Identify the blood parasite species.
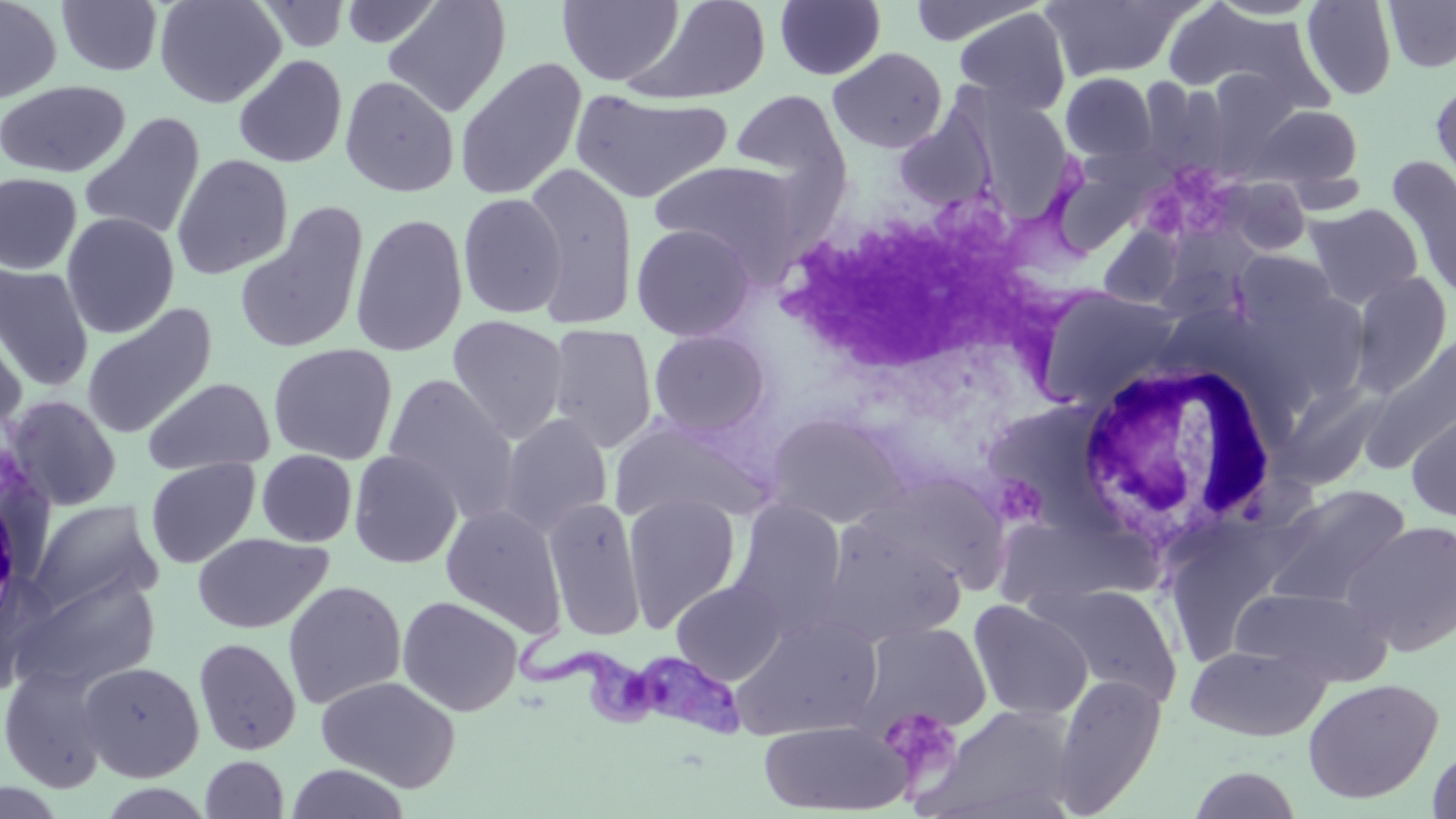
Trypanosoma brucei.

Summary:
  - Coordinate format: approximate bounding boxes as [x1, y1, x2, y2] in pixels
  - White blood cell locations: [768, 183, 1078, 387], [1072, 356, 1283, 562]
  - Platelet locations: [879, 706, 963, 787]
  - Uninfected red blood cell locations: [0, 0, 62, 104], [154, 0, 286, 109], [382, 0, 511, 118], [557, 0, 684, 87], [625, 0, 772, 106], [1040, 0, 1195, 82], [1206, 0, 1324, 20], [1301, 0, 1397, 100], [1384, 0, 1456, 73], [56, 1, 164, 76], [254, 1, 353, 52], [341, 1, 442, 48], [775, 1, 886, 81], [906, 1, 1038, 47], [1161, 2, 1310, 99], [953, 8, 1072, 117], [828, 47, 948, 153], [233, 54, 348, 168], [454, 57, 587, 202], [1060, 72, 1158, 163], [340, 75, 459, 197], [0, 80, 131, 179], [1430, 81, 1456, 203], [569, 89, 732, 204], [730, 89, 850, 191], [972, 96, 1076, 215], [1248, 104, 1363, 189], [78, 111, 206, 241], [893, 111, 996, 211], [172, 153, 293, 279], [1041, 153, 1156, 258], [1387, 156, 1456, 303], [649, 160, 804, 276], [522, 164, 639, 328], [0, 172, 82, 275], [1214, 176, 1312, 257], [769, 181, 1052, 388], [457, 193, 567, 319], [234, 202, 369, 355], [1305, 203, 1423, 309], [61, 212, 180, 338], [350, 212, 468, 357], [631, 223, 757, 342], [1097, 225, 1183, 309], [1233, 250, 1338, 336], [0, 263, 95, 391], [1349, 270, 1453, 398], [1033, 288, 1184, 409], [82, 303, 217, 439], [0, 314, 28, 446], [447, 315, 569, 444], [546, 324, 658, 453], [648, 328, 772, 439], [1362, 334, 1456, 474], [268, 343, 398, 464], [382, 374, 520, 522], [143, 378, 275, 476], [1272, 382, 1391, 492], [4, 395, 122, 511], [1406, 402, 1456, 523], [765, 410, 909, 529], [499, 413, 613, 538], [607, 414, 772, 527], [256, 449, 358, 547], [348, 450, 463, 569], [145, 458, 260, 569], [854, 472, 1012, 590], [1262, 484, 1412, 609], [623, 493, 741, 630], [544, 496, 646, 642], [730, 497, 848, 633], [28, 499, 161, 616], [441, 505, 566, 638], [819, 517, 965, 646], [1343, 519, 1456, 656], [192, 533, 333, 633], [17, 574, 159, 691], [671, 579, 787, 684], [282, 580, 406, 709], [1037, 583, 1183, 709], [1231, 585, 1393, 686], [397, 596, 523, 716], [968, 599, 1093, 721], [730, 614, 883, 740], [857, 621, 992, 736], [194, 637, 301, 756], [1185, 644, 1330, 741], [78, 661, 205, 782], [1, 664, 111, 793], [1051, 674, 1167, 816], [316, 675, 460, 792], [1302, 677, 1444, 804], [925, 702, 1080, 818], [759, 719, 910, 814], [1426, 741, 1456, 818], [200, 755, 289, 818], [285, 763, 411, 819], [1187, 766, 1305, 819]
  - Trypanosoma brucei locations: [513, 620, 746, 739]
  - Magnification: 1000x
  - Stain: May-Grünwald-Giemsa
  - Preparation: thin blood film
  - Modality: optical microscopy
  - Field of view: single
  - Image size: 1456×819 pixels